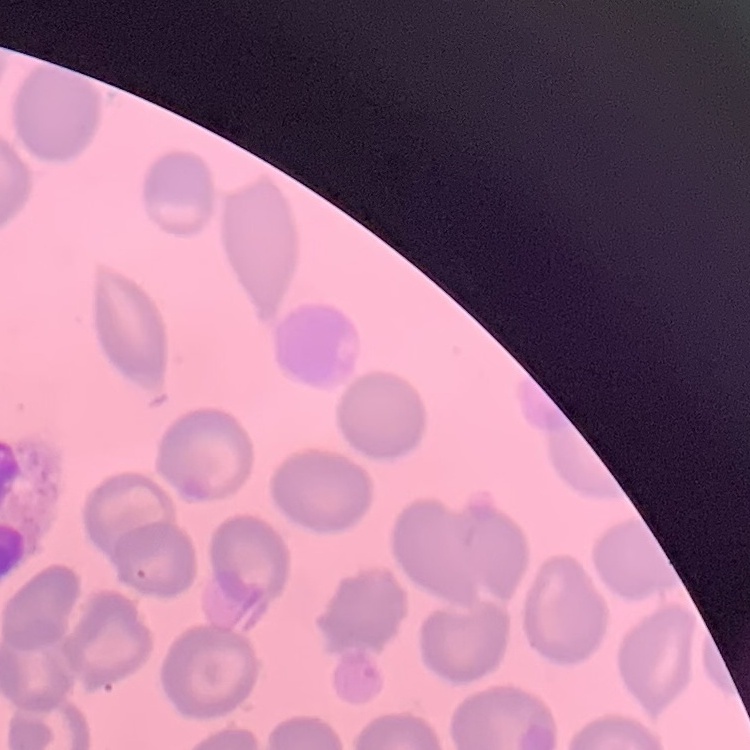
erythrocyte morphology = no rouleaux formation
preparation = thin blood smear
stain = Field's or Giemsa
image type = one tile cut from a larger photomicrograph